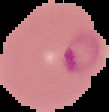
From a thin blood film. Cell region segmented out of the field of view; the surrounding area is masked to black. Malaria status: parasitized. Image is 109×112 pixels.